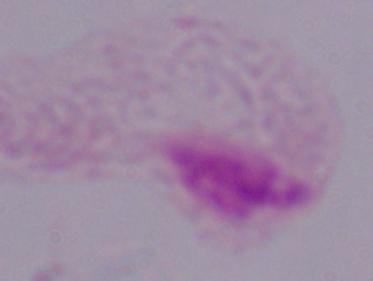
identification = trichomonad
magnification = 1000x
modality = micrograph